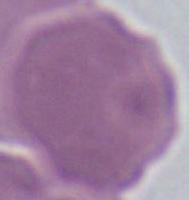

magnification: 1000x
modality: micrograph
identification: erythrocyte